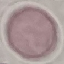
Summary:
  - Malaria status: uninfected
  - Image type: cell patch, automatically extracted from a larger field of view and resized to 64 × 64 pixels
  - Preparation: thin blood film
  - Capture: smartphone camera at the microscope eyepiece
  - Stain: Giemsa